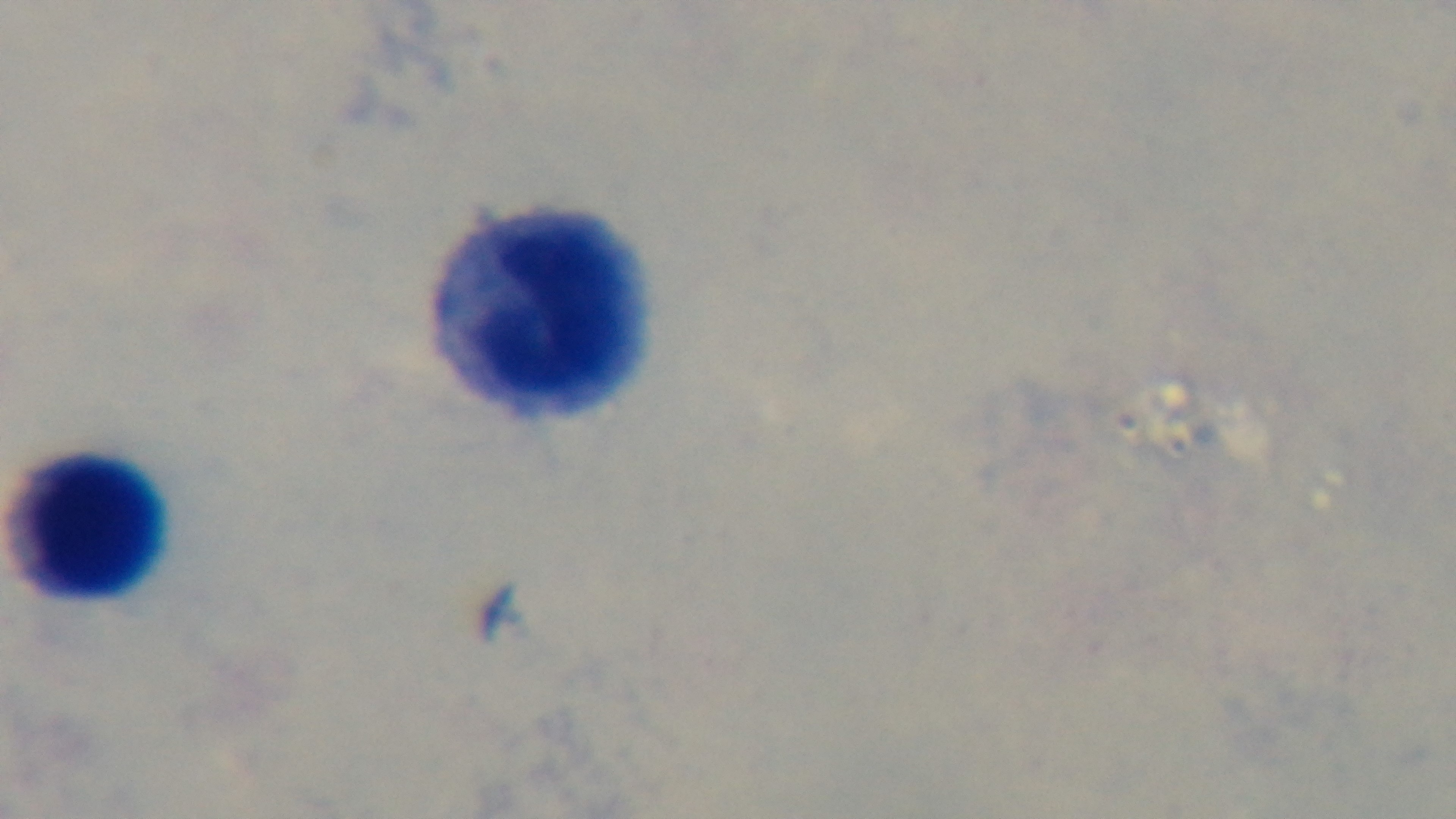

field of view = single
modality = light microscopy
objective = 100x oil immersion
preparation = thick blood film
stain = Giemsa
malaria status = negative
capture = mounted 4K digital camera